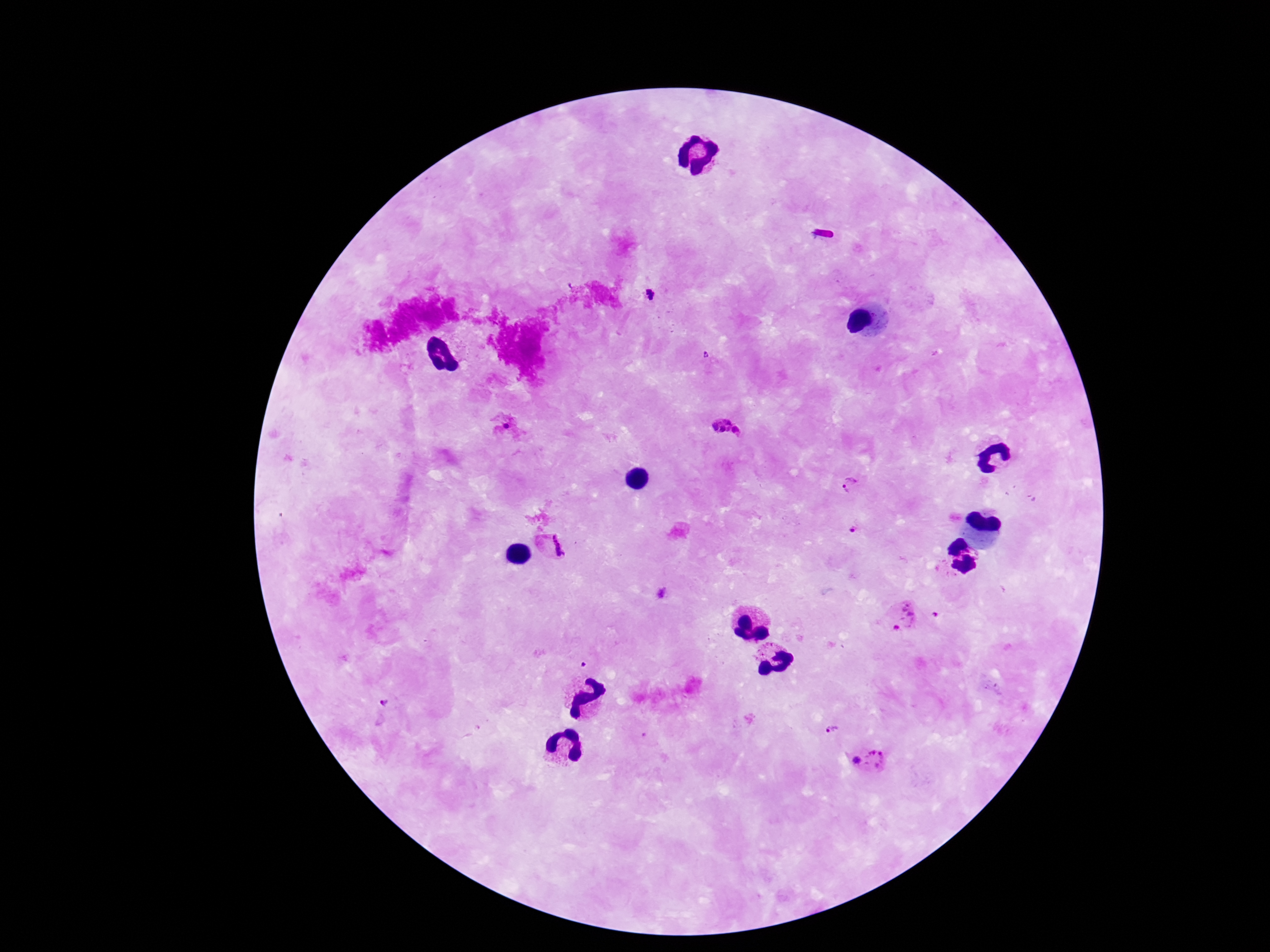

Approximate object centers, in pixels from the top-left corner. Plasmodium parasite locations: (x=649, y=293), (x=708, y=355), (x=727, y=428), (x=851, y=484), (x=854, y=530), (x=551, y=543), (x=937, y=612), (x=902, y=618), (x=388, y=701), (x=829, y=727), (x=869, y=759). Smartphone photograph taken through the microscope eyepiece. Image is 1270×952 pixels. Patient malaria status: infected. Thick blood smear. Giemsa stain. 100x magnification. Single field of view.